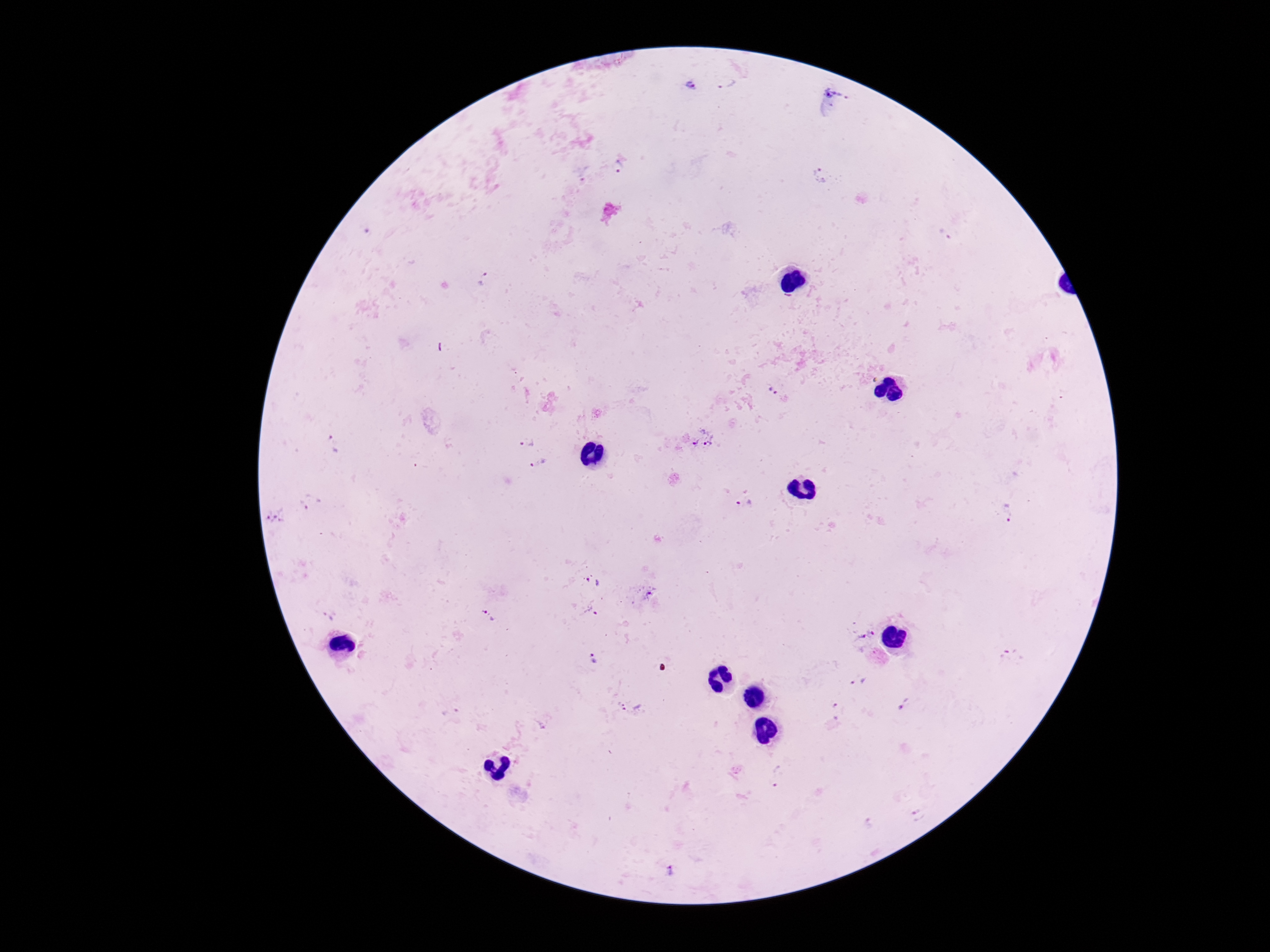
Approximate centers as [x, y] in pixels.
Summary:
  - Plasmodium parasite locations: [726, 82], [691, 86], [835, 94], [619, 167], [820, 175], [946, 234], [483, 279], [773, 392], [703, 438], [528, 442], [333, 443], [537, 463], [745, 502], [309, 503], [1008, 512], [276, 516], [593, 583], [644, 594], [592, 611], [489, 615], [329, 617], [873, 630], [859, 642], [594, 658], [858, 682], [904, 704], [631, 707], [837, 711], [452, 713], [540, 725], [777, 776], [918, 815], [868, 824], [671, 870]
  - Preparation: thick peripheral-blood smear
  - Field of view: one from this slide
  - Capture: smartphone camera through the microscope eyepiece
  - Image size: 1270×952 pixels
  - Magnification: 100x
  - Stain: Giemsa
  - Patient malaria status: positive